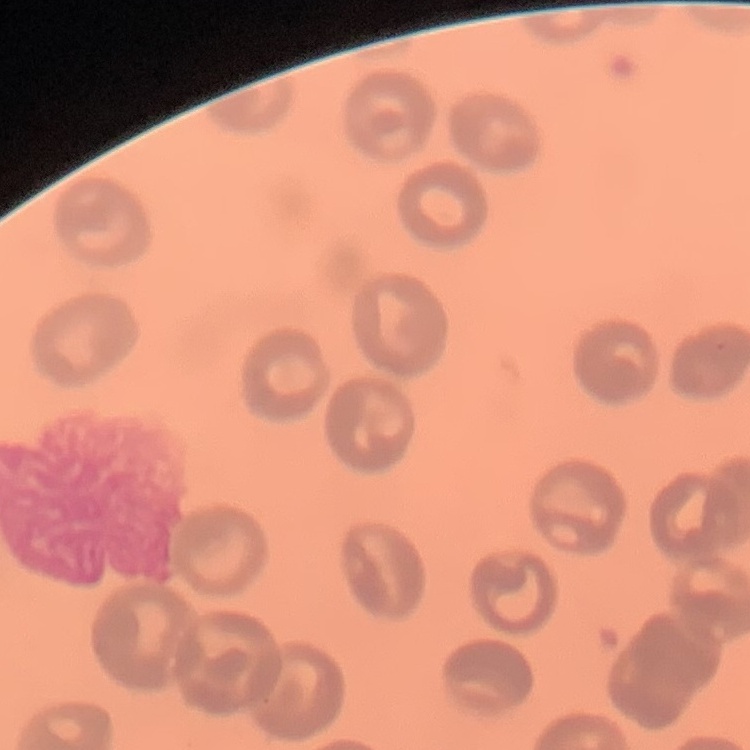

Summary:
  - Erythrocyte morphology: no rouleaux formation
  - Preparation: thin peripheral smear
  - Image type: one tile cut from a larger photomicrograph
  - Stain: Field's or Giemsa